Locate every Plasmodium ovale-infected red blood cell.
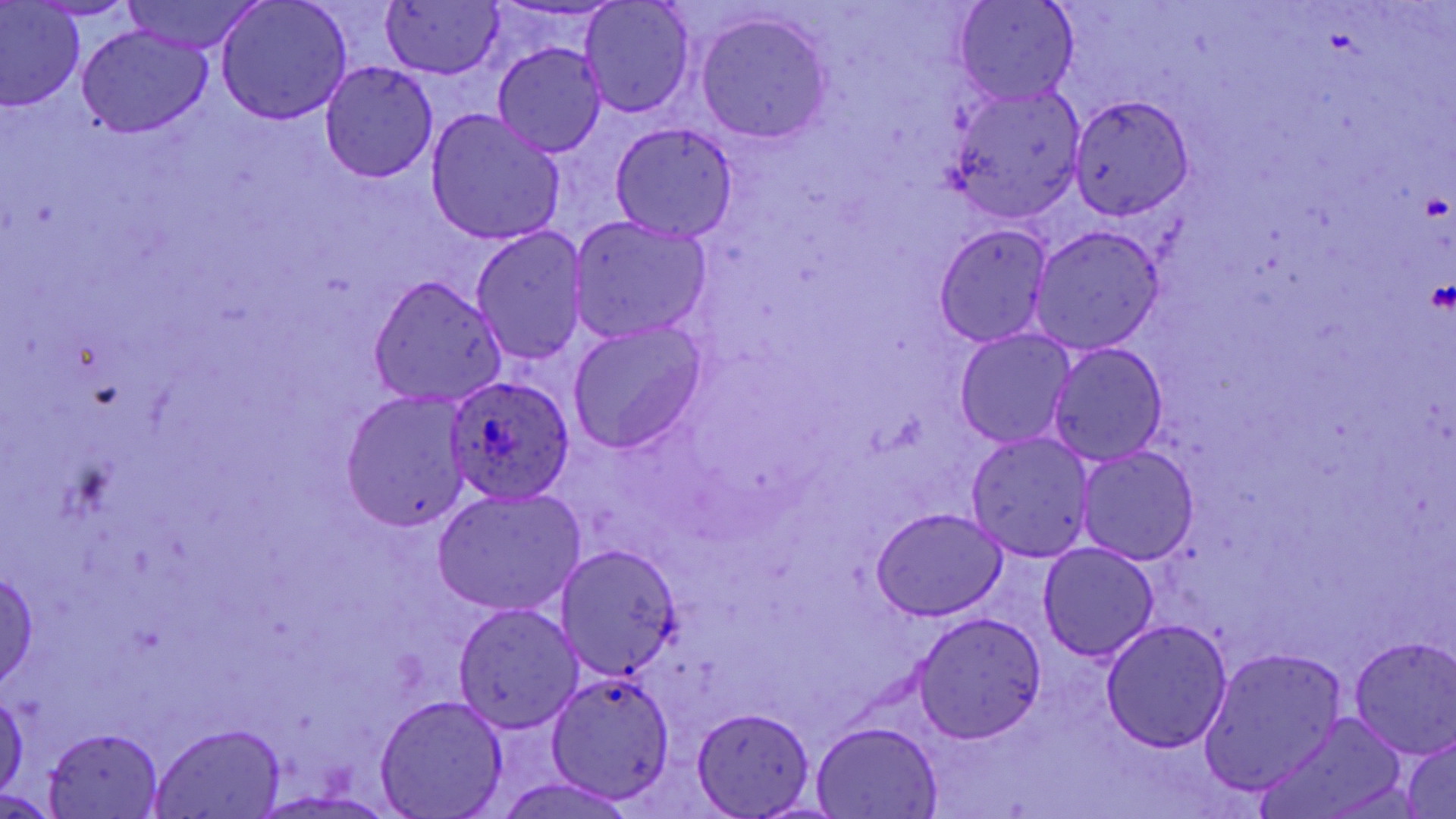

Approximate bounding boxes as [x1, y1, x2, y2] in pixels.
Plasmodium ovale-infected red blood cells: [443, 374, 574, 505].

Summary:
  - Uninfected red blood cell locations: [120, 0, 264, 53], [953, 0, 1078, 107], [30, 1, 136, 20], [580, 1, 695, 119], [216, 2, 352, 124], [381, 3, 502, 79], [1, 4, 83, 109], [697, 13, 832, 142], [77, 25, 212, 136], [492, 43, 607, 158], [321, 63, 437, 183], [947, 87, 1085, 224], [1068, 95, 1195, 220], [425, 109, 566, 246], [609, 122, 739, 242], [569, 216, 713, 344], [932, 224, 1053, 346], [471, 227, 587, 365], [1030, 227, 1163, 353], [370, 277, 508, 406], [567, 320, 708, 454], [955, 328, 1075, 448], [1047, 341, 1169, 467], [342, 390, 469, 534], [965, 432, 1097, 561], [1077, 447, 1199, 565], [434, 487, 586, 616], [871, 507, 1007, 621], [1037, 543, 1159, 661], [556, 544, 681, 677], [0, 568, 40, 688], [452, 603, 585, 733], [913, 612, 1046, 743], [1102, 620, 1232, 752], [1348, 636, 1456, 758], [1200, 646, 1348, 795], [544, 672, 677, 801], [0, 691, 27, 800], [375, 696, 509, 817], [692, 705, 816, 817], [1261, 714, 1409, 819], [810, 722, 943, 817], [150, 724, 286, 818], [42, 726, 166, 818], [1401, 733, 1456, 818], [490, 776, 641, 819], [252, 790, 392, 817], [0, 791, 59, 816]
  - Platelet locations: [1419, 191, 1450, 222], [1425, 277, 1455, 316]
  - Slide-level diagnosis: Plasmodium ovale
  - Modality: optical microscopy
  - Field of view: one of a larger specimen
  - Image size: 1456×819 pixels
  - Stain: May-Grünwald-Giemsa
  - Preparation: thin blood film
  - Magnification: 1000x